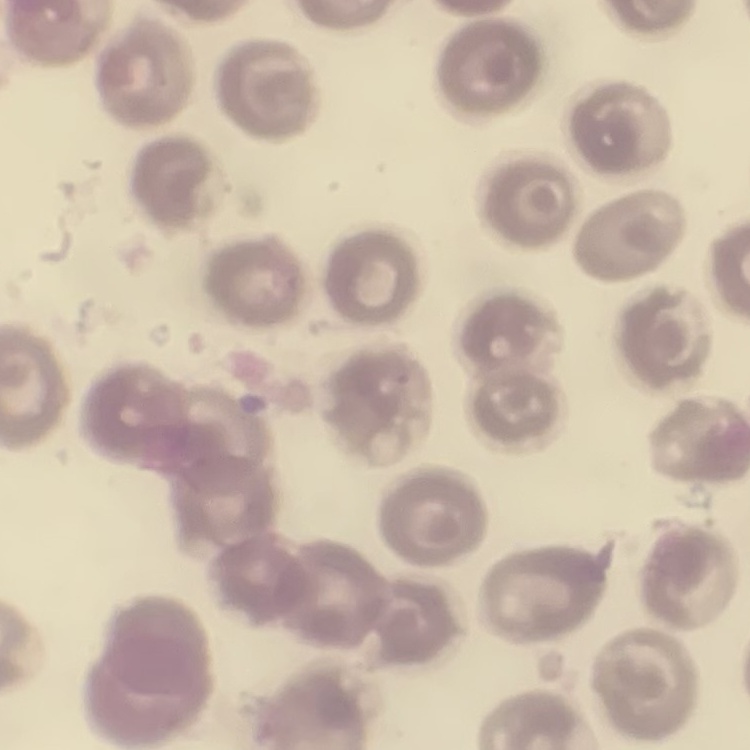
Summary:
  - Red blood cell morphology: no rouleaux formation
  - Stain: Field's or Giemsa
  - Preparation: thin peripheral smear
  - Image type: square crop of a larger photomicrograph